Identify the parasite.
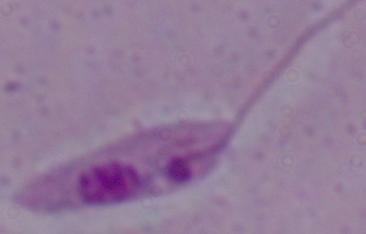

Leishmania.

1000x magnification. Photomicrograph.